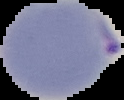

Summary:
  - Malaria status: parasitized
  - Image size: 124×100 pixels
  - Image type: segmented cell region on a black background
  - Preparation: thin blood smear